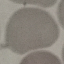
{
  "result": "no malaria parasites seen",
  "preparation": "thin blood film",
  "capture": "smartphone through the microscope eyepiece",
  "image_type": "automatically extracted cell patch, resized to 64 × 64 pixels",
  "stain": "Giemsa"
}